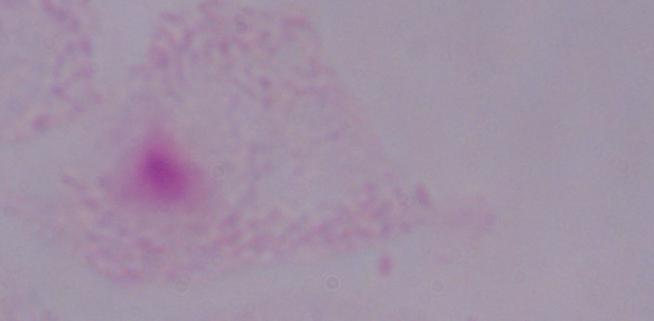
{
  "magnification": "1000x",
  "identification": "trichomonad",
  "modality": "micrograph"
}